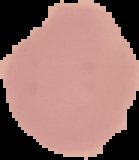 Image is 139×160 pixels. From a thin blood film. Malaria status: uninfected. Cell region segmented out of the field of view; the surrounding area is masked to black.